Name the cell type shown.
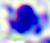

A leukocyte.

Captured at 400x magnification. Photomicrograph.